Identify the parasite.
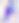

Toxoplasma gondii.

Micrograph. Captured at 400x magnification.